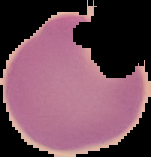

malaria status = uninfected
image type = cell region segmented out of the field of view; surrounding area masked to black
preparation = thin blood film
image size = 151×157 pixels